Name the parasite shown.
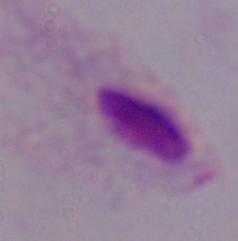

This is a trichomonad.

modality = photomicrograph
magnification = 1000x